Classify this cell by malaria status.
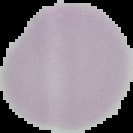

It is uninfected.

preparation = thin blood film
image size = 133×133 pixels
image type = segmented cell region on a black background